Give the extent of all Plasmodium falciparum-infected red blood cells.
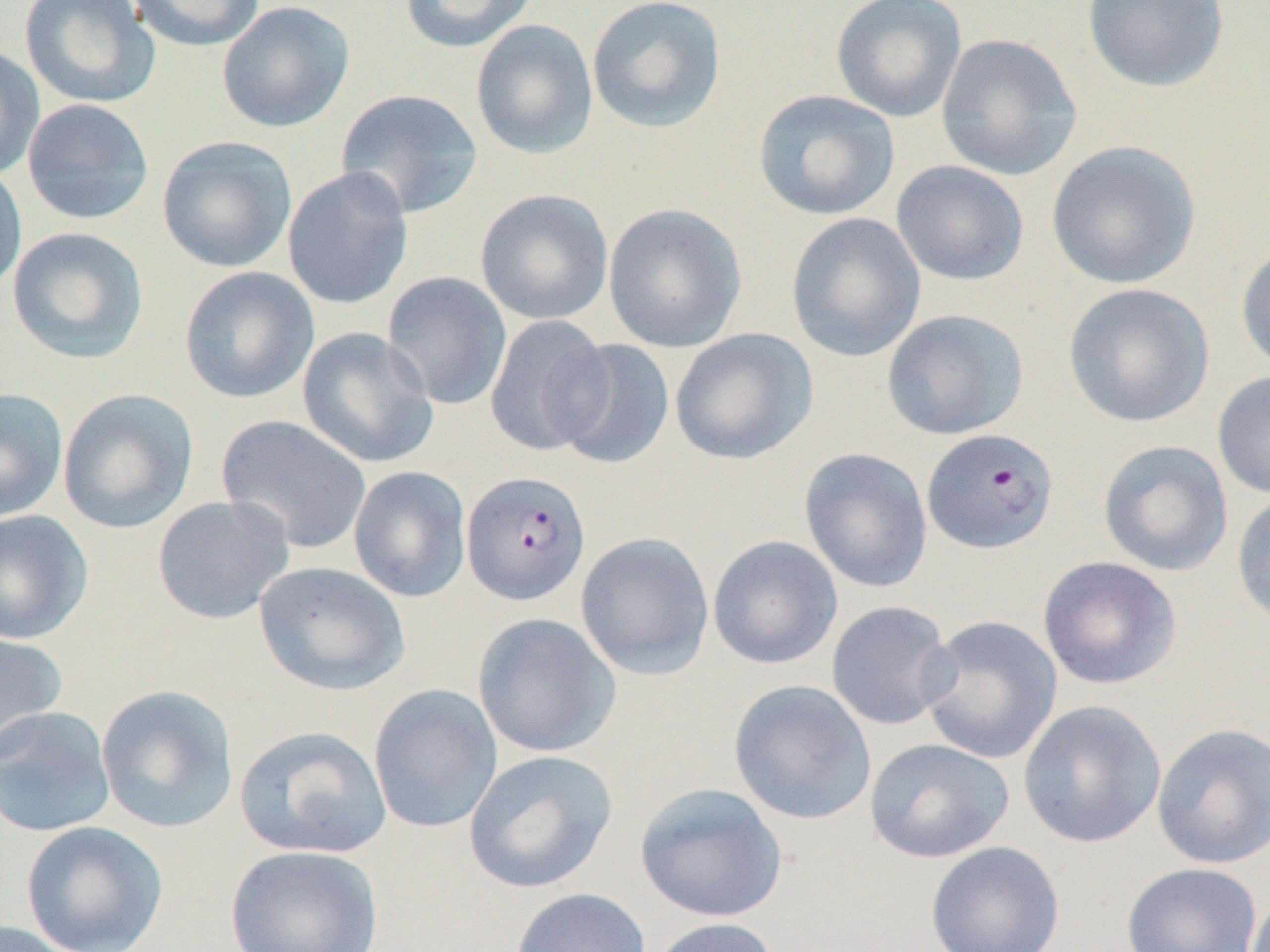

Approximate bounding boxes as (x1, y1, x2, y2) in pixels.
Plasmodium falciparum-infected red blood cells: (921, 428, 1059, 555), (461, 470, 592, 606).

slide-level diagnosis = Plasmodium falciparum
field of view = single
preparation = thin blood smear
magnification = 1000x
uninfected red blood cell locations = approximate bounding boxes as (x1, y1, x2, y2) in pixels: (19, 0, 160, 109), (128, 0, 265, 52), (400, 0, 538, 54), (586, 0, 727, 134), (830, 0, 967, 123), (1081, 0, 1230, 93), (216, 1, 355, 133), (470, 19, 599, 160), (935, 33, 1082, 181), (0, 44, 45, 181), (336, 89, 483, 220), (753, 89, 900, 221), (22, 98, 155, 225), (157, 135, 297, 273), (1045, 140, 1201, 290), (0, 160, 28, 299), (890, 160, 1030, 287), (282, 166, 414, 310), (474, 188, 614, 326), (602, 202, 747, 354), (785, 212, 927, 362), (7, 226, 149, 364), (1235, 242, 1270, 376), (178, 266, 320, 405), (381, 271, 513, 410), (1062, 282, 1215, 428), (881, 309, 1029, 441), (484, 314, 613, 456), (297, 327, 439, 469), (669, 327, 818, 465), (550, 338, 676, 470), (1212, 369, 1270, 500), (0, 387, 68, 522), (57, 389, 199, 534), (215, 415, 372, 555), (1097, 440, 1234, 577), (799, 447, 933, 594), (348, 466, 472, 603), (1231, 490, 1270, 628), (151, 495, 296, 625), (0, 509, 93, 645), (575, 531, 715, 680), (707, 535, 844, 671), (1037, 555, 1182, 690), (253, 561, 411, 696), (825, 600, 958, 731), (472, 612, 622, 758), (918, 614, 1063, 765), (0, 632, 68, 763), (728, 679, 877, 825), (368, 683, 503, 833), (95, 684, 240, 834), (1016, 700, 1166, 848), (0, 705, 117, 839), (1151, 723, 1270, 869), (233, 724, 392, 859), (864, 737, 1016, 864), (462, 749, 618, 894), (633, 783, 789, 923), (21, 820, 168, 952), (925, 840, 1065, 952), (224, 844, 384, 952), (1121, 862, 1263, 952), (510, 887, 652, 952), (1247, 888, 1270, 952), (645, 917, 781, 952), (0, 920, 82, 952)
modality = light microscopy
image size = 1270×952 pixels